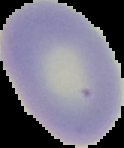

From a thin blood film. Segmented cell region on a black background. Malaria status: uninfected. Image is 124×148 pixels.